Comment on the morphology of the red blood cells.
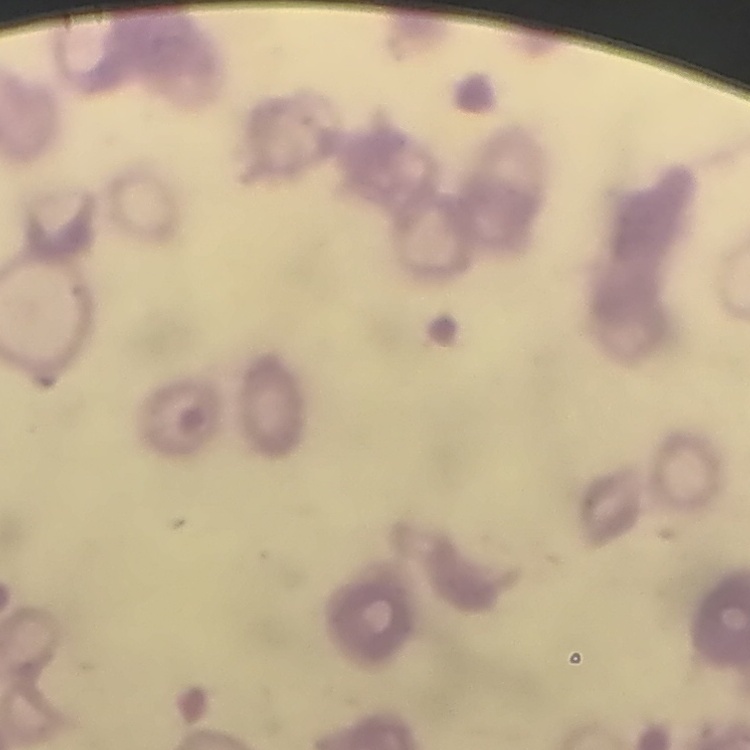

Rouleaux formation.

Summary:
  - Stain: Field's or Giemsa
  - Preparation: thin blood smear
  - Image type: square crop of a larger photomicrograph